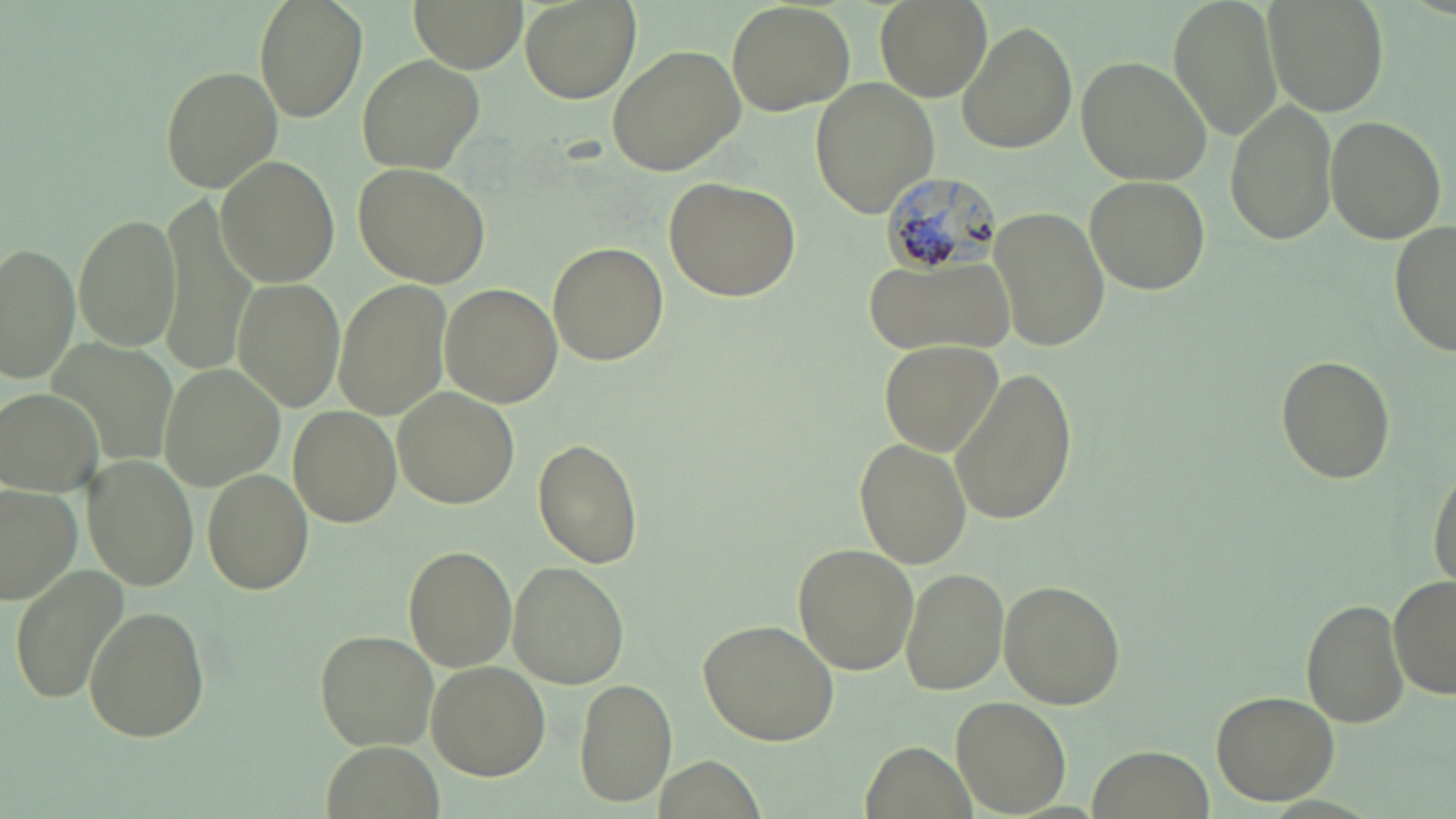 Approximate bounding boxes as [x1, y1, x2, y2] in pixels. Uninfected red blood cell locations: [255, 0, 366, 118], [414, 0, 524, 70], [519, 0, 639, 104], [876, 0, 990, 102], [1170, 0, 1284, 141], [1261, 0, 1386, 115], [728, 2, 854, 115], [955, 22, 1077, 155], [606, 44, 746, 177], [359, 55, 485, 174], [1075, 55, 1212, 187], [159, 65, 283, 190], [810, 77, 941, 218], [1224, 98, 1341, 247], [1323, 115, 1447, 245], [217, 157, 341, 288], [354, 163, 491, 287], [663, 176, 802, 302], [1083, 176, 1210, 294], [156, 200, 257, 375], [990, 204, 1108, 352], [74, 212, 181, 353], [1388, 218, 1456, 360], [0, 242, 80, 381], [548, 242, 668, 366], [862, 255, 1015, 356], [232, 276, 345, 412], [334, 280, 450, 420], [439, 283, 562, 407], [879, 338, 1001, 456], [1273, 352, 1397, 484], [159, 362, 286, 491], [949, 363, 1079, 528], [391, 387, 520, 509], [2, 388, 104, 495], [287, 405, 400, 526], [854, 437, 973, 569], [532, 439, 644, 569], [83, 456, 199, 591], [1427, 460, 1456, 590], [203, 469, 314, 593], [0, 484, 83, 606], [790, 543, 918, 671], [403, 547, 516, 671], [505, 562, 630, 689], [9, 566, 128, 705], [900, 568, 1010, 695], [1391, 572, 1455, 702], [998, 580, 1126, 708], [1301, 598, 1410, 729], [84, 605, 209, 741], [699, 620, 842, 746], [315, 629, 438, 752], [423, 662, 548, 779], [574, 679, 677, 807], [1210, 688, 1341, 804], [951, 695, 1072, 818], [320, 738, 441, 819], [862, 740, 974, 819], [1092, 746, 1213, 816]. Plasmodium malariae-infected red blood cell locations: [878, 173, 1000, 280]. Slide-level diagnosis: Plasmodium malariae. Image is 1456×819 pixels. Thin blood film. May-Grünwald-Giemsa stain. 1000x magnification. Optical microscopy. Single field of view.